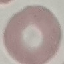
Result: negative for malaria parasites. Thin smear of blood. Cell patch, automatically extracted from a larger field of view and resized to 64 × 64 pixels. Giemsa-stained preparation. Photographed with a smartphone camera at the microscope eyepiece.